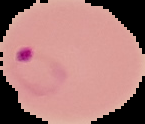
image type = segmented cell region on a black background
image size = 145×124 pixels
preparation = thin blood smear
result = malaria parasites identified